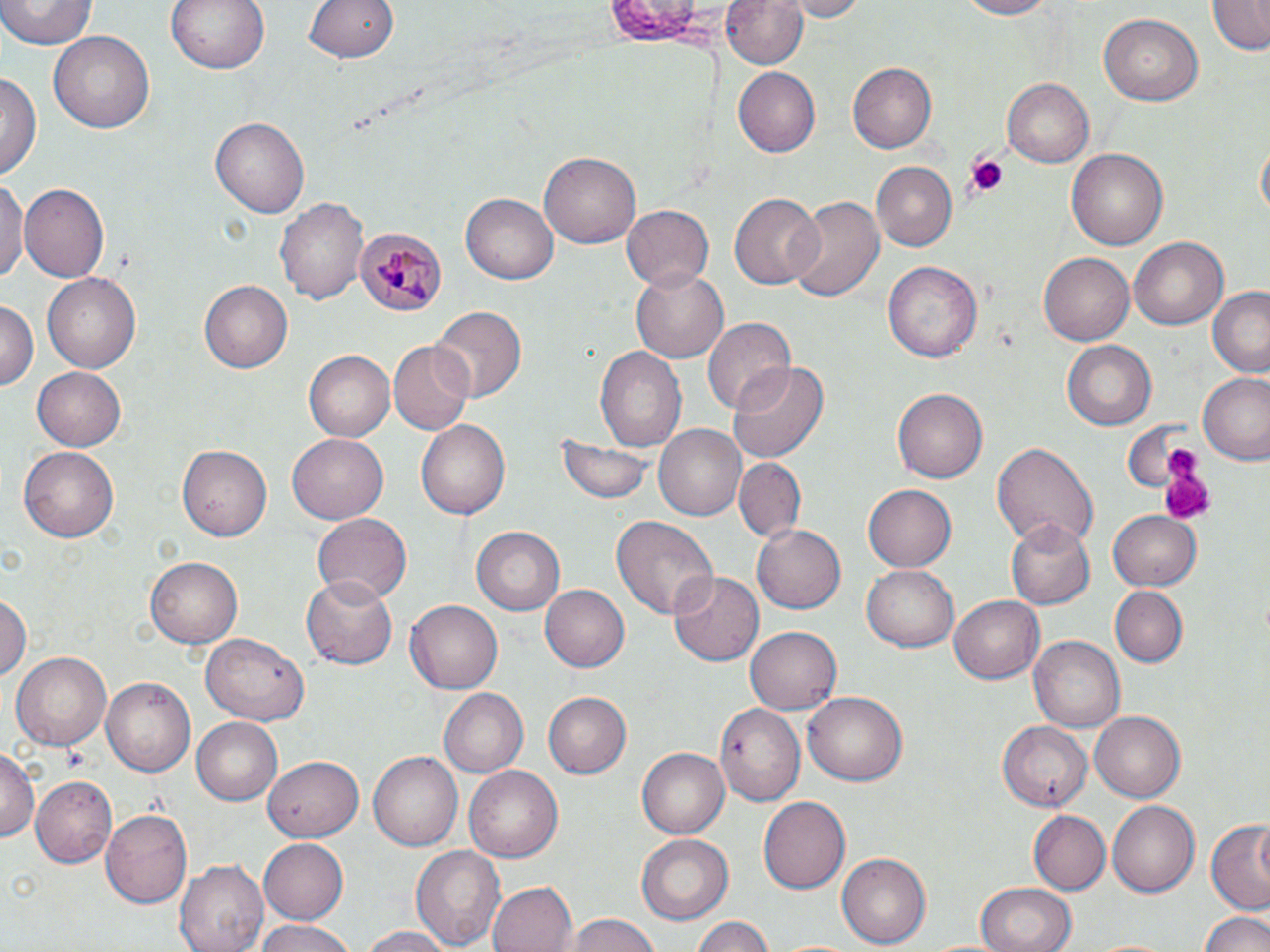
Summary:
  - Coordinate format: approximate bounding boxes as named x1/y1/x2/y2 corners in pixels
  - Plasmodium malariae-infected red blood cell locations: (x1=357, y1=229, x2=444, y2=316)
  - Platelet locations: (x1=958, y1=154, x2=1010, y2=203), (x1=1158, y1=452, x2=1217, y2=525)
  - Uninfected red blood cell locations: (x1=0, y1=0, x2=96, y2=52), (x1=164, y1=0, x2=271, y2=76), (x1=304, y1=0, x2=400, y2=63), (x1=724, y1=0, x2=810, y2=70), (x1=780, y1=0, x2=866, y2=20), (x1=950, y1=0, x2=1063, y2=20), (x1=596, y1=2, x2=728, y2=43), (x1=1208, y1=2, x2=1268, y2=55), (x1=1098, y1=11, x2=1203, y2=106), (x1=48, y1=30, x2=155, y2=132), (x1=848, y1=61, x2=938, y2=154), (x1=733, y1=68, x2=820, y2=155), (x1=0, y1=71, x2=40, y2=183), (x1=1000, y1=77, x2=1095, y2=167), (x1=211, y1=115, x2=310, y2=220), (x1=1256, y1=138, x2=1269, y2=226), (x1=1067, y1=148, x2=1168, y2=252), (x1=541, y1=150, x2=640, y2=248), (x1=869, y1=160, x2=956, y2=249), (x1=0, y1=178, x2=25, y2=286), (x1=20, y1=181, x2=108, y2=283), (x1=730, y1=193, x2=821, y2=289), (x1=460, y1=194, x2=558, y2=285), (x1=785, y1=195, x2=884, y2=306), (x1=276, y1=196, x2=370, y2=307), (x1=620, y1=205, x2=714, y2=291), (x1=1127, y1=237, x2=1229, y2=331), (x1=1038, y1=252, x2=1134, y2=347), (x1=884, y1=260, x2=982, y2=364), (x1=629, y1=264, x2=727, y2=363), (x1=41, y1=272, x2=143, y2=372), (x1=199, y1=279, x2=292, y2=373), (x1=1208, y1=289, x2=1270, y2=378), (x1=0, y1=298, x2=38, y2=397), (x1=432, y1=307, x2=524, y2=402), (x1=701, y1=314, x2=796, y2=417), (x1=1061, y1=339, x2=1158, y2=431), (x1=389, y1=341, x2=474, y2=434), (x1=594, y1=346, x2=687, y2=450), (x1=304, y1=350, x2=394, y2=440), (x1=729, y1=361, x2=830, y2=465), (x1=30, y1=365, x2=125, y2=451), (x1=1198, y1=372, x2=1270, y2=466), (x1=893, y1=386, x2=988, y2=483), (x1=418, y1=420, x2=509, y2=520), (x1=655, y1=424, x2=746, y2=521), (x1=287, y1=434, x2=389, y2=524), (x1=551, y1=434, x2=655, y2=507), (x1=671, y1=436, x2=801, y2=528), (x1=990, y1=442, x2=1099, y2=553), (x1=18, y1=444, x2=119, y2=540), (x1=177, y1=445, x2=272, y2=541), (x1=734, y1=457, x2=805, y2=543), (x1=864, y1=482, x2=957, y2=571), (x1=1107, y1=510, x2=1201, y2=592), (x1=310, y1=513, x2=412, y2=605), (x1=611, y1=516, x2=717, y2=623), (x1=1005, y1=520, x2=1094, y2=609), (x1=752, y1=522, x2=845, y2=615), (x1=471, y1=525, x2=565, y2=614), (x1=145, y1=556, x2=243, y2=647), (x1=862, y1=567, x2=958, y2=652), (x1=670, y1=572, x2=763, y2=665), (x1=300, y1=573, x2=401, y2=672), (x1=540, y1=583, x2=628, y2=672), (x1=1110, y1=585, x2=1187, y2=667), (x1=0, y1=593, x2=30, y2=685), (x1=948, y1=594, x2=1045, y2=684), (x1=404, y1=599, x2=502, y2=695), (x1=746, y1=625, x2=845, y2=715), (x1=201, y1=634, x2=310, y2=725), (x1=1030, y1=637, x2=1124, y2=731), (x1=9, y1=649, x2=112, y2=750), (x1=103, y1=676, x2=195, y2=779), (x1=439, y1=688, x2=528, y2=777), (x1=542, y1=691, x2=631, y2=780), (x1=803, y1=692, x2=908, y2=786), (x1=715, y1=703, x2=804, y2=805), (x1=1089, y1=710, x2=1185, y2=802), (x1=193, y1=718, x2=283, y2=806), (x1=997, y1=720, x2=1093, y2=811), (x1=1, y1=745, x2=39, y2=843), (x1=637, y1=747, x2=730, y2=839), (x1=369, y1=751, x2=462, y2=851), (x1=262, y1=755, x2=363, y2=841), (x1=465, y1=766, x2=563, y2=863), (x1=30, y1=775, x2=116, y2=869), (x1=758, y1=795, x2=850, y2=895), (x1=1105, y1=800, x2=1198, y2=899), (x1=101, y1=809, x2=193, y2=907), (x1=1027, y1=810, x2=1110, y2=896), (x1=1205, y1=820, x2=1269, y2=911), (x1=637, y1=834, x2=733, y2=922), (x1=260, y1=837, x2=350, y2=925), (x1=409, y1=844, x2=507, y2=952), (x1=836, y1=852, x2=930, y2=949), (x1=175, y1=859, x2=269, y2=952), (x1=487, y1=880, x2=575, y2=952), (x1=975, y1=882, x2=1073, y2=952), (x1=1199, y1=908, x2=1270, y2=952), (x1=563, y1=914, x2=665, y2=952), (x1=689, y1=916, x2=777, y2=952), (x1=252, y1=919, x2=355, y2=952), (x1=354, y1=926, x2=456, y2=952)
  - Slide-level diagnosis: Plasmodium malariae
  - Modality: optical microscopy
  - Stain: May-Grünwald-Giemsa
  - Image size: 1270×952 pixels
  - Preparation: thin blood smear
  - Magnification: 1000x
  - Field of view: one of a larger specimen